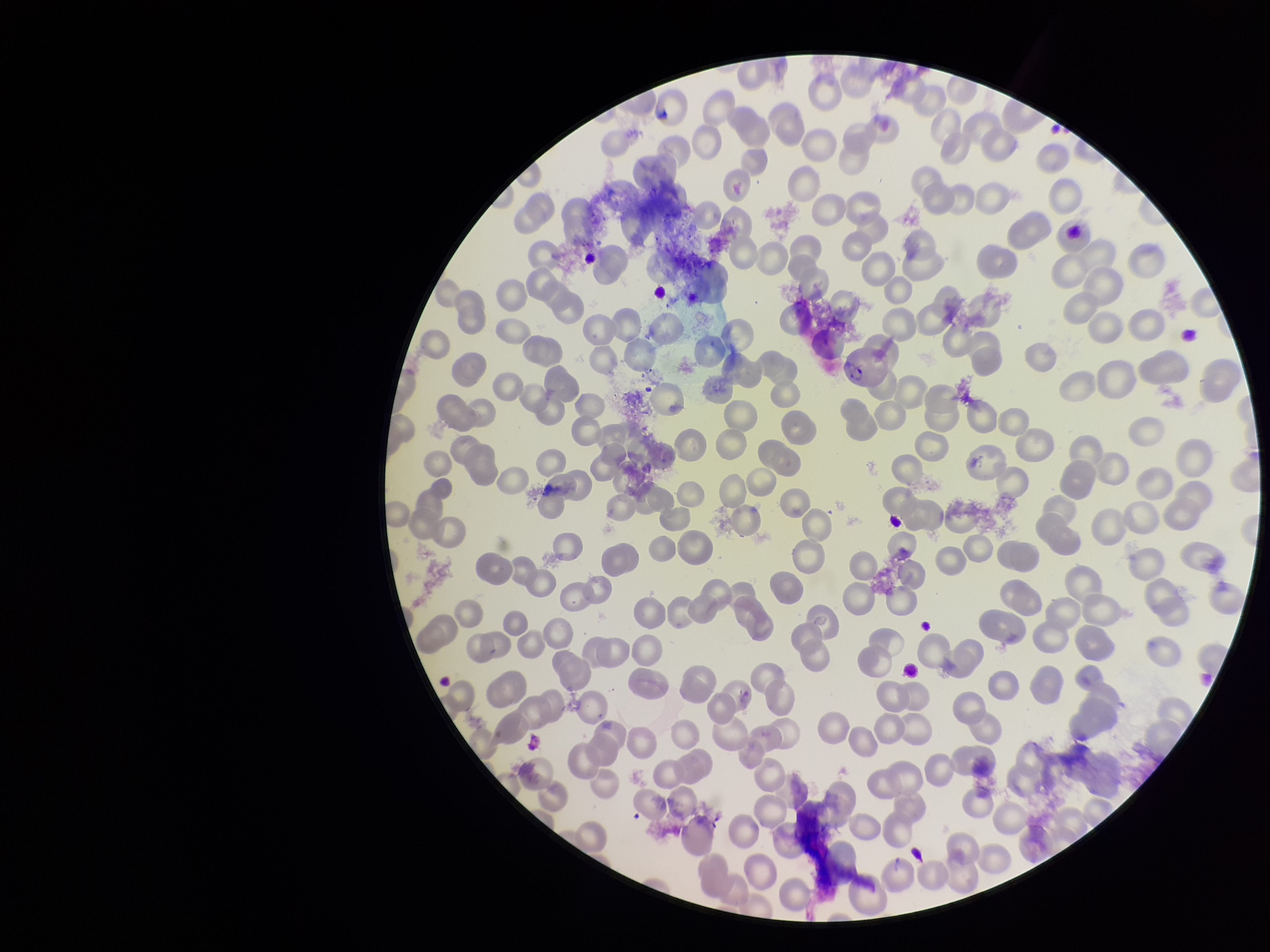

Image is 1270×952 pixels. Species reported for this patient: Plasmodium vivax. Parasitized red blood cells: none seen. One field from this slide. Red blood cell count: 228. Smartphone photograph taken through the eyepiece of a microscope. Patient malaria status: positive. Preparation: thin. Stained with Giemsa. Parasitized red blood cell count: 0.